Classify this cell by malaria status.
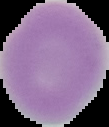
Uninfected.

image size = 109×127 pixels
image type = cell region segmented out of the field of view; surrounding area masked to black
preparation = thin blood film